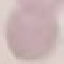
Summary:
  - Malaria status: uninfected
  - Preparation: thin blood film
  - Stain: Giemsa
  - Image type: automatically extracted cell patch, resized to 64 × 64 pixels
  - Capture: smartphone camera at the microscope eyepiece